Name the blood parasite species.
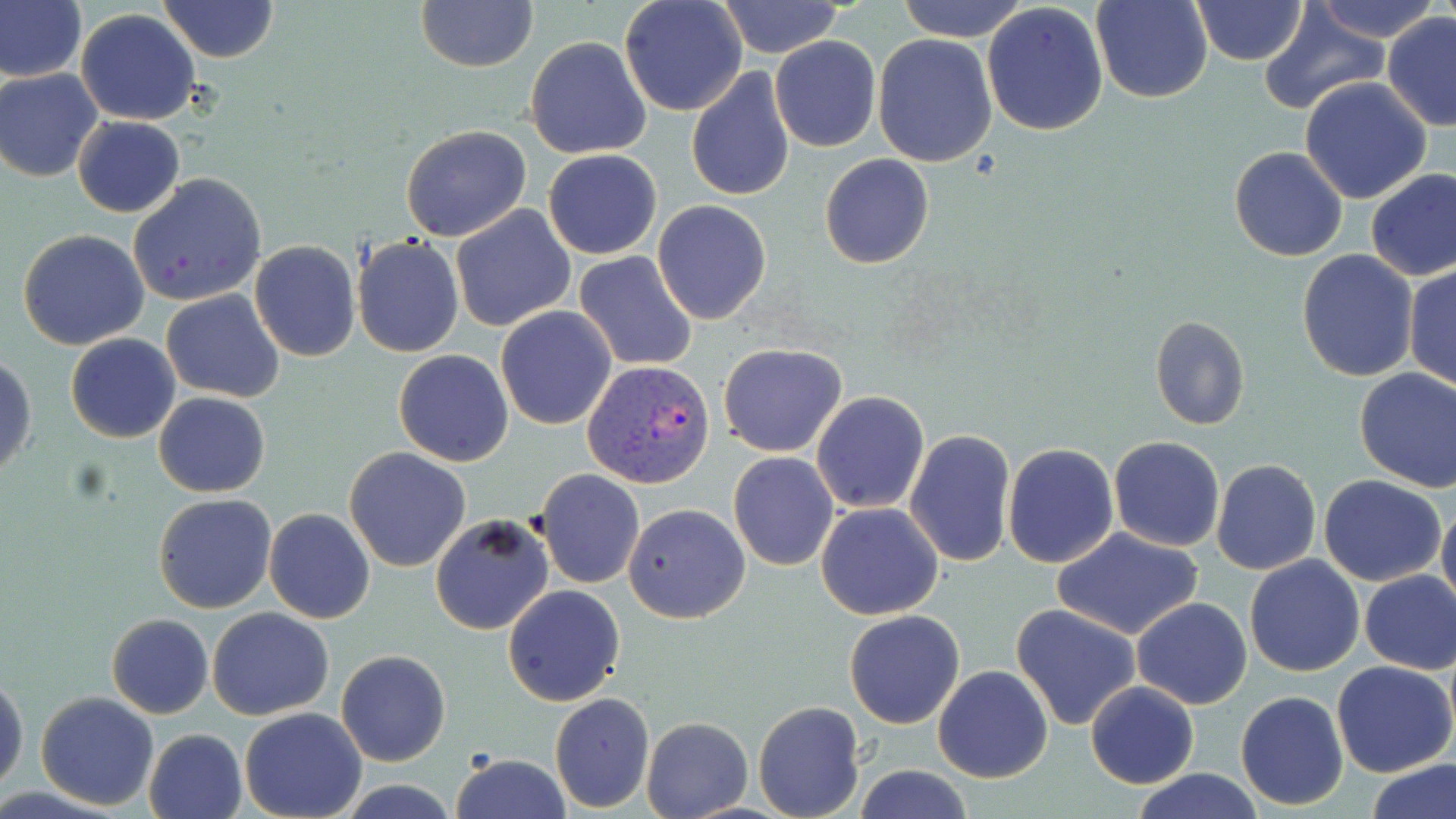

Plasmodium vivax.

Summary:
  - Coordinate format: approximate bounding boxes as (x1, y1, x2, y2) in pixels
  - Uninfected red blood cell locations: (159, 0, 278, 63), (619, 0, 747, 117), (897, 0, 1027, 42), (1091, 0, 1213, 103), (1312, 0, 1441, 43), (415, 1, 538, 71), (715, 1, 847, 57), (1190, 1, 1308, 66), (0, 2, 86, 82), (982, 3, 1109, 136), (1254, 8, 1391, 115), (75, 9, 203, 126), (1381, 12, 1456, 129), (873, 34, 999, 167), (770, 35, 881, 152), (525, 36, 652, 159), (684, 68, 795, 200), (1, 69, 103, 181), (1301, 77, 1433, 205), (72, 116, 185, 218), (399, 125, 532, 243), (1228, 146, 1348, 262), (543, 149, 662, 259), (819, 153, 934, 269), (1364, 168, 1456, 283), (127, 172, 268, 308), (652, 200, 772, 324), (450, 205, 577, 332), (17, 229, 149, 350), (352, 236, 465, 356), (247, 240, 362, 362), (574, 251, 699, 371), (1297, 251, 1418, 381), (1404, 262, 1455, 391), (161, 289, 286, 402), (495, 306, 616, 431), (1149, 316, 1251, 433), (65, 333, 181, 443), (718, 343, 848, 458), (393, 350, 514, 466), (0, 354, 37, 480), (1353, 367, 1456, 492), (153, 391, 270, 496), (810, 391, 929, 512), (903, 429, 1015, 566), (1108, 437, 1226, 552), (1002, 444, 1118, 567), (345, 448, 471, 572), (728, 452, 840, 571), (1211, 459, 1322, 575), (535, 468, 645, 589), (1319, 475, 1448, 587), (152, 492, 277, 613), (1436, 498, 1456, 619), (815, 501, 944, 620), (624, 502, 750, 623), (264, 508, 374, 623), (430, 514, 555, 636), (1051, 526, 1205, 642), (1244, 555, 1365, 677), (1358, 570, 1456, 674), (503, 584, 625, 707), (1133, 597, 1251, 710), (1012, 603, 1142, 729), (206, 607, 334, 720), (844, 608, 966, 728), (107, 613, 214, 718), (336, 649, 452, 766), (1332, 660, 1456, 777), (933, 665, 1052, 783), (0, 669, 27, 795), (1086, 682, 1199, 789), (1235, 690, 1350, 811), (34, 691, 160, 809), (549, 692, 654, 814), (753, 700, 864, 819), (240, 708, 366, 819), (641, 716, 754, 819), (144, 728, 248, 819), (450, 752, 572, 819), (1367, 759, 1456, 819), (855, 765, 975, 819), (1127, 768, 1267, 819)
  - Plasmodium vivax-infected red blood cell locations: (581, 359, 716, 489)
  - Preparation: thin blood smear
  - Magnification: 1000x
  - Field of view: single
  - Modality: light microscopy
  - Stain: May-Grünwald-Giemsa
  - Image size: 1456×819 pixels